Point out each leukocyte.
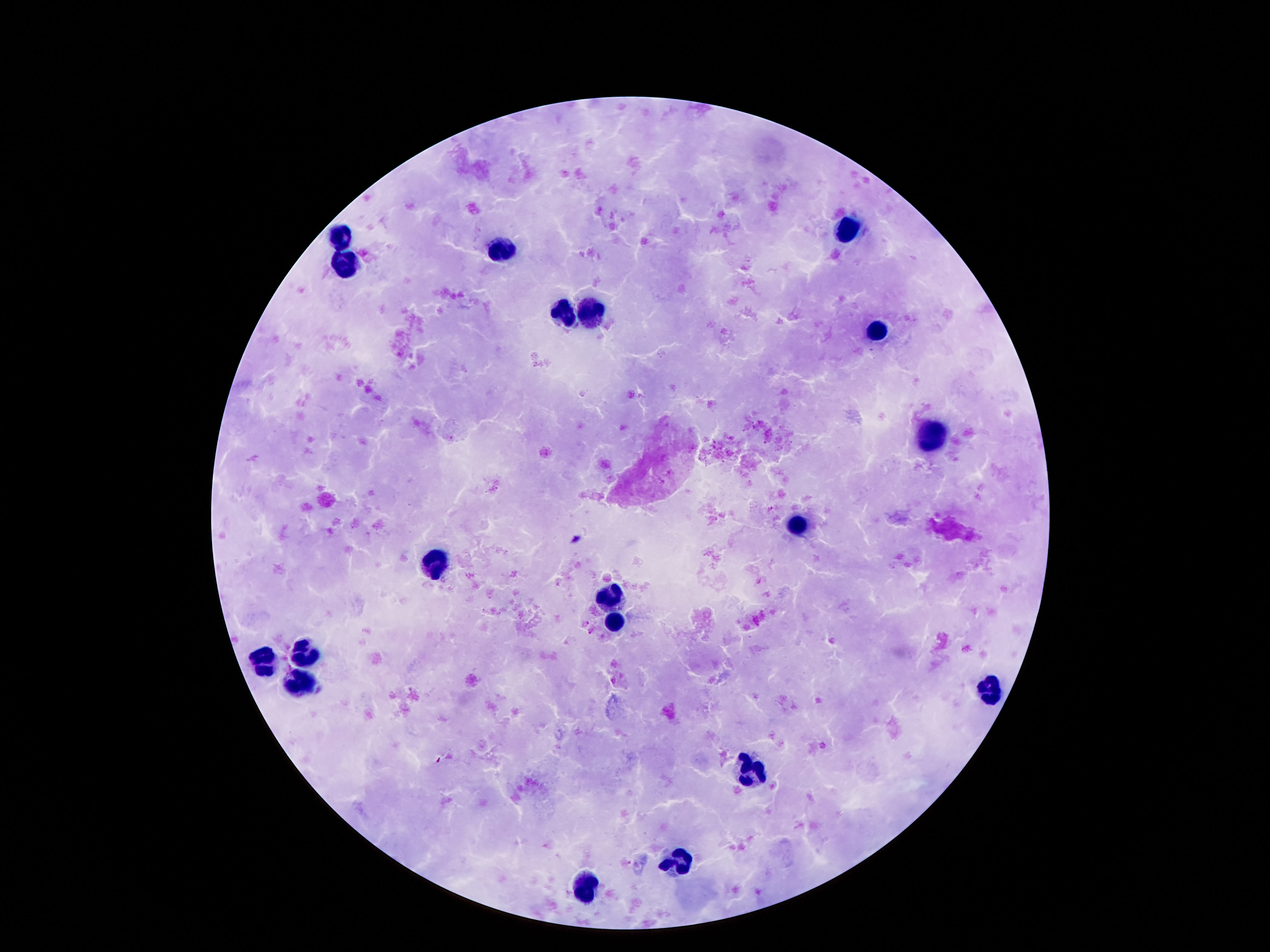

Approximate centers as {x, y} in pixels.
Leukocytes: {846, 229}, {342, 234}, {504, 249}, {349, 260}, {594, 310}, {565, 314}, {876, 330}, {931, 436}, {795, 526}, {439, 561}, {611, 596}, {615, 621}, {304, 652}, {267, 663}, {300, 683}, {986, 688}, {754, 772}, {678, 860}, {589, 885}.

Photographed through the microscope eyepiece with a smartphone camera. Image is 1270×952 pixels. Single field of view. 100x magnification. Patient malaria status: negative. Thick blood smear. Giemsa-stained preparation.